Classify this cell by malaria status.
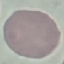

Uninfected.

{
  "image_type": "cell patch, automatically extracted from a larger field of view and resized to 64 × 64 pixels",
  "stain": "Giemsa",
  "preparation": "thin blood film",
  "capture": "smartphone through the microscope eyepiece"
}